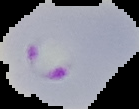
{
  "image_size": "139×109 pixels",
  "preparation": "thin blood smear",
  "image_type": "segmented cell region on a black background",
  "malaria_status": "parasitized"
}